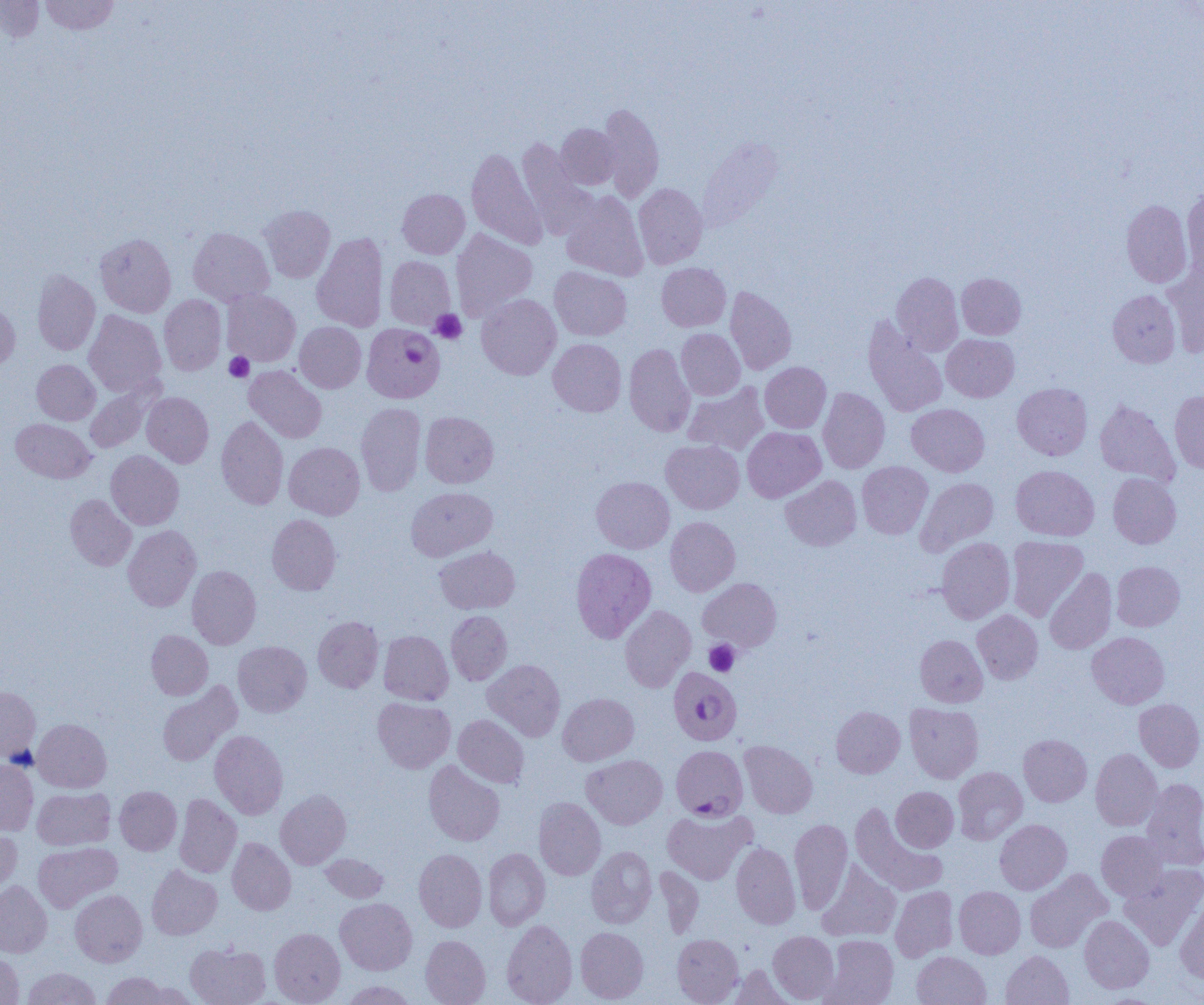 Approximate bounding boxes as (x1, y1, x2, y2) in pixels. Uninfected red blood cell locations: (0, 0, 45, 43), (39, 0, 120, 35), (597, 103, 664, 202), (555, 123, 621, 189), (517, 137, 594, 237), (467, 148, 547, 249), (633, 183, 708, 269), (1183, 186, 1204, 274), (397, 189, 470, 258), (561, 191, 648, 281), (1121, 199, 1192, 287), (259, 205, 335, 283), (188, 227, 274, 306), (451, 228, 537, 320), (312, 232, 389, 332), (95, 233, 176, 317), (384, 256, 456, 330), (1163, 260, 1204, 357), (657, 263, 731, 331), (549, 266, 632, 341), (32, 269, 100, 355), (891, 272, 963, 356), (957, 273, 1026, 339), (725, 286, 796, 375), (222, 290, 300, 366), (1107, 290, 1180, 368), (476, 294, 561, 380), (159, 295, 226, 375), (0, 303, 20, 374), (84, 310, 166, 396), (863, 317, 947, 417), (295, 322, 366, 393), (676, 329, 745, 400), (942, 334, 1019, 402), (548, 338, 626, 416), (624, 343, 695, 436), (32, 359, 100, 425), (760, 362, 831, 432), (244, 365, 326, 443), (85, 382, 158, 453), (683, 382, 769, 455), (1012, 383, 1092, 460), (818, 387, 890, 473), (1170, 390, 1204, 473), (142, 392, 213, 467), (1095, 399, 1179, 485), (356, 403, 426, 496), (907, 403, 989, 476), (420, 411, 498, 488), (216, 416, 289, 509), (11, 418, 95, 483), (742, 427, 825, 502), (661, 440, 744, 514), (284, 442, 364, 519), (106, 450, 184, 529), (857, 461, 933, 539), (1011, 465, 1099, 540), (1108, 473, 1181, 548), (781, 475, 861, 550), (591, 476, 674, 553), (916, 477, 998, 555), (406, 486, 497, 561), (65, 494, 136, 570), (267, 514, 341, 595), (665, 517, 740, 596), (123, 525, 201, 611), (1007, 536, 1087, 621), (936, 537, 1015, 623), (434, 546, 520, 613), (570, 548, 656, 643), (1111, 561, 1184, 631), (187, 566, 261, 649), (1044, 568, 1117, 654), (698, 578, 781, 651), (620, 606, 696, 692), (972, 609, 1043, 684), (446, 611, 512, 685), (313, 616, 383, 692), (146, 630, 213, 700), (379, 630, 453, 705), (1087, 632, 1169, 708), (915, 634, 987, 707), (233, 641, 312, 717), (483, 659, 565, 741), (157, 683, 240, 766), (0, 686, 40, 761), (558, 693, 639, 765), (372, 697, 455, 773), (1134, 699, 1204, 772), (905, 703, 983, 783), (831, 706, 905, 778), (453, 714, 529, 788), (33, 719, 111, 792), (210, 730, 288, 819), (1018, 734, 1092, 806), (739, 740, 818, 818), (1091, 748, 1162, 830), (582, 755, 667, 829), (0, 759, 38, 836), (424, 760, 504, 846), (953, 767, 1027, 844), (1141, 778, 1204, 870), (114, 786, 182, 855), (891, 786, 958, 852), (32, 787, 115, 850), (275, 789, 351, 869), (174, 794, 242, 877), (534, 796, 606, 880), (850, 803, 947, 896), (662, 808, 756, 885), (789, 818, 852, 913), (995, 819, 1071, 894), (0, 828, 22, 894), (1096, 830, 1168, 901), (227, 838, 296, 915), (33, 842, 122, 912), (731, 842, 801, 929), (586, 846, 657, 928), (483, 848, 550, 931), (414, 849, 487, 932), (320, 853, 389, 903), (817, 862, 900, 941), (1120, 864, 1204, 950), (146, 865, 222, 940), (654, 867, 704, 938), (1024, 869, 1111, 952), (0, 881, 52, 957), (890, 886, 958, 962), (954, 886, 1025, 958), (70, 889, 147, 966), (1176, 896, 1204, 984), (335, 898, 417, 975), (1079, 915, 1154, 993), (501, 919, 577, 1005), (575, 927, 649, 1003), (269, 928, 345, 1004), (768, 931, 839, 1003), (672, 933, 743, 1004), (421, 935, 490, 1005), (822, 935, 898, 1005), (185, 942, 271, 1005), (1001, 950, 1074, 1005), (912, 951, 991, 1005), (0, 952, 24, 1004), (728, 964, 795, 1004), (22, 967, 102, 1004), (101, 972, 170, 1004), (137, 981, 199, 1004), (340, 981, 418, 1004). Platelet locations: (430, 310, 467, 344), (224, 352, 254, 382), (704, 640, 740, 677). Plasmodium falciparum-infected red blood cell locations: (363, 323, 443, 402), (667, 669, 744, 745), (671, 745, 748, 820). Slide-level diagnosis: Plasmodium falciparum. Thin blood film. Image is 1204×1005 pixels. Captured at 1000x magnification. Optical microscopy. One field of a larger specimen.